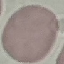
Result: negative for malaria parasites. Giemsa-stained preparation. Photographed with a smartphone camera at the microscope eyepiece. Thin smear of blood. Automatically extracted cell patch, resized to 64 × 64 pixels.